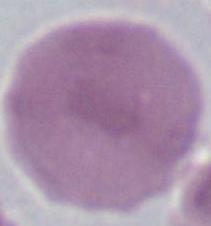
magnification = 1000x
modality = micrograph
identification = red blood cell